Mark where leukocytes are.
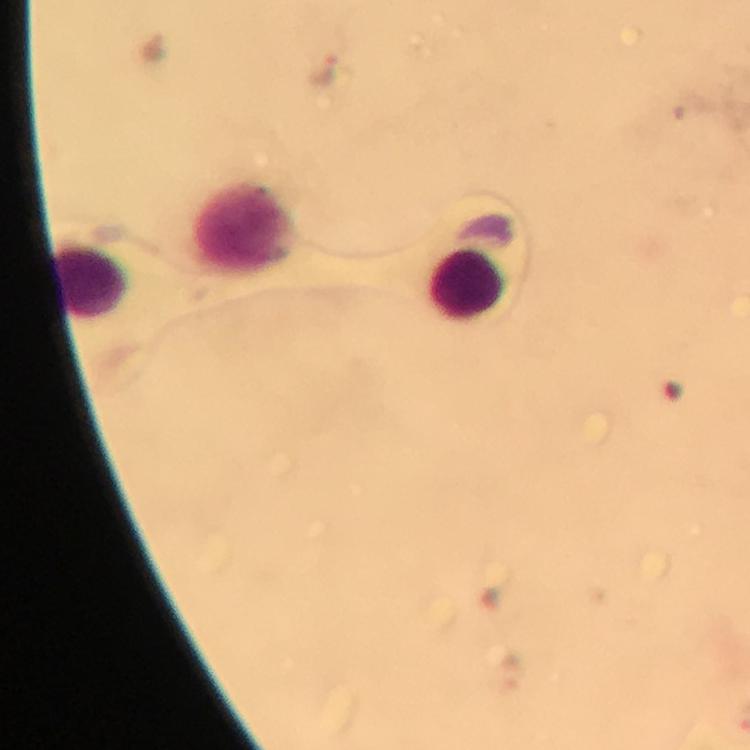

Approximate centers as (x, y) in pixels.
Leukocytes: (246, 227), (90, 281), (466, 285).

preparation = thick smear
cropped from = one field of view
capture = smartphone camera through the microscope
stain = Giemsa
context = from a malaria diagnostic workup
Plasmodium parasite locations = approximate centers as (x, y) in pixels: (322, 74)
image size = 750×750 pixels
immersion oil = applied
magnification = 100x